Describe the morphology of the red blood cells.
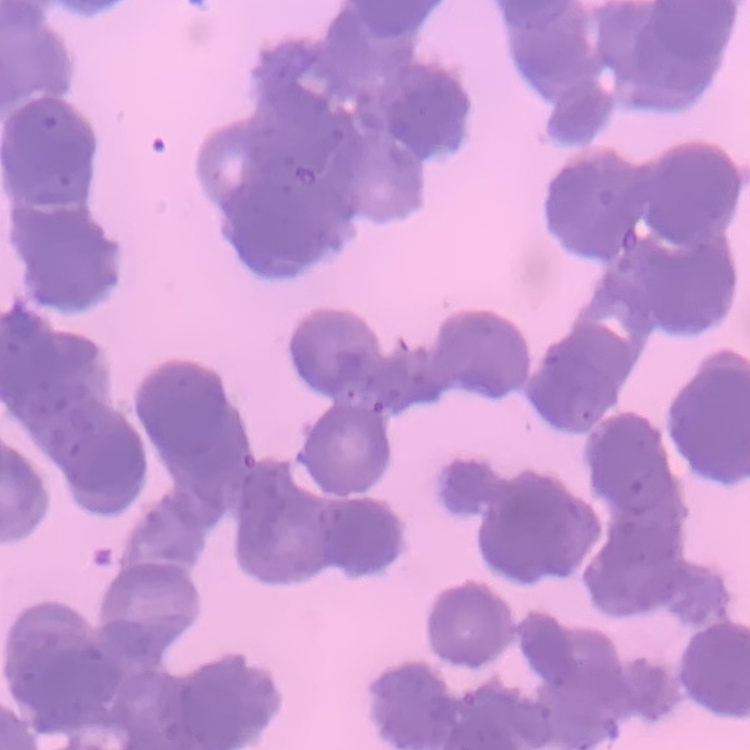

They show rouleaux formation.

Summary:
  - Stain: Field's or Giemsa
  - Image type: one tile cut from a larger photomicrograph
  - Preparation: thin blood film